Point out malaria parasites and leukocytes.
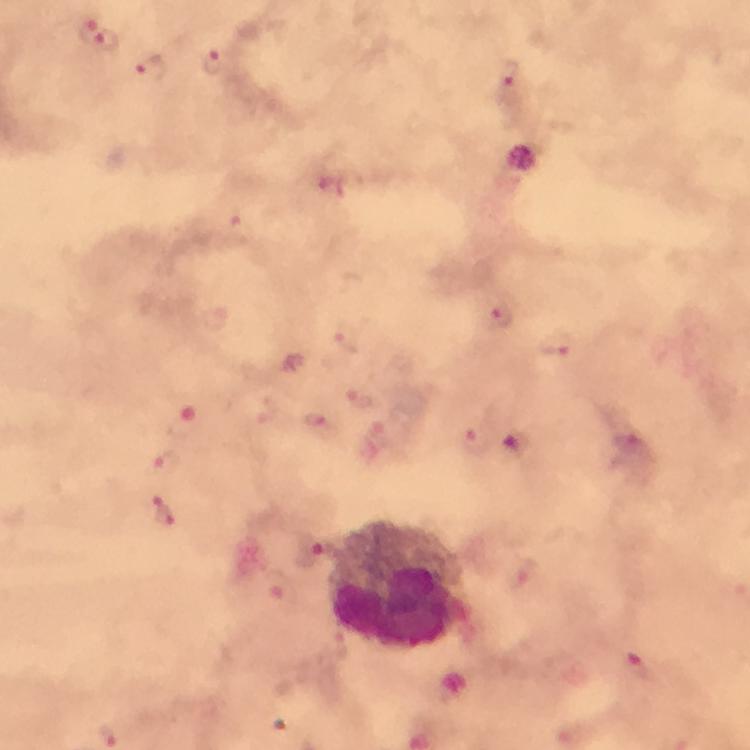
Approximate centers as [x, y] in pixels.
Malaria parasites: [100, 39], [215, 67], [154, 69], [508, 73], [238, 230], [501, 316], [346, 338], [553, 349], [360, 398], [321, 427], [475, 441], [515, 442], [168, 464], [165, 511], [314, 553], [638, 666].
Leukocytes: [402, 586].

Summary:
  - Context: from a malaria diagnostic workup
  - Capture: smartphone camera through the microscope
  - Stain: Giemsa
  - Cropped from: one field of view
  - Preparation: thick blood smear
  - Image size: 750×750 pixels
  - Magnification: 100x
  - Immersion oil: used